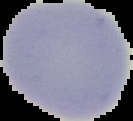

image_size: 133×121 pixels
image_type: segmented cell region with the area outside set to black
malaria_status: uninfected
preparation: thin blood film